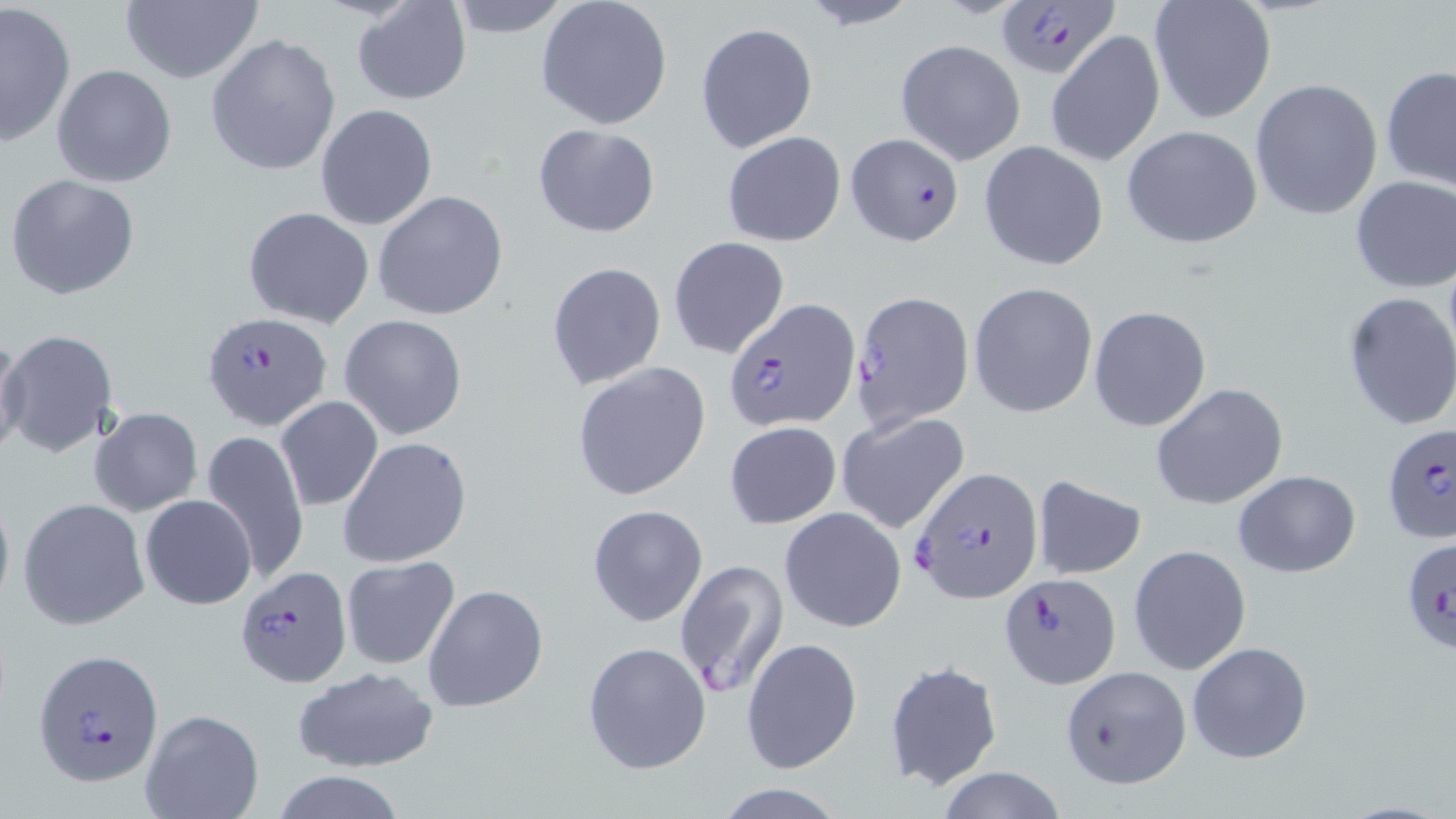 Approximate bounding boxes as named x1/y1/x2/y2 corners in pixels. Uninfected red blood cell locations: (x1=351, y1=0, x2=472, y2=105), (x1=444, y1=0, x2=574, y2=36), (x1=1149, y1=0, x2=1276, y2=123), (x1=0, y1=1, x2=76, y2=147), (x1=119, y1=1, x2=263, y2=85), (x1=536, y1=1, x2=672, y2=129), (x1=793, y1=2, x2=924, y2=30), (x1=695, y1=22, x2=818, y2=153), (x1=1046, y1=31, x2=1165, y2=167), (x1=205, y1=33, x2=342, y2=179), (x1=895, y1=39, x2=1025, y2=165), (x1=51, y1=64, x2=178, y2=187), (x1=1381, y1=64, x2=1456, y2=194), (x1=1250, y1=77, x2=1384, y2=221), (x1=314, y1=104, x2=438, y2=230), (x1=531, y1=123, x2=660, y2=238), (x1=1121, y1=125, x2=1264, y2=249), (x1=721, y1=131, x2=846, y2=246), (x1=979, y1=140, x2=1109, y2=271), (x1=6, y1=174, x2=140, y2=300), (x1=1350, y1=176, x2=1455, y2=292), (x1=372, y1=189, x2=510, y2=321), (x1=244, y1=206, x2=374, y2=327), (x1=666, y1=236, x2=790, y2=357), (x1=547, y1=261, x2=667, y2=392), (x1=968, y1=282, x2=1098, y2=417), (x1=1340, y1=291, x2=1456, y2=434), (x1=1088, y1=307, x2=1212, y2=431), (x1=340, y1=314, x2=467, y2=441), (x1=2, y1=329, x2=120, y2=458), (x1=0, y1=332, x2=28, y2=462), (x1=571, y1=362, x2=713, y2=500), (x1=1151, y1=382, x2=1288, y2=509), (x1=276, y1=396, x2=383, y2=511), (x1=88, y1=406, x2=203, y2=516), (x1=835, y1=412, x2=970, y2=534), (x1=724, y1=420, x2=842, y2=528), (x1=201, y1=430, x2=311, y2=582), (x1=338, y1=436, x2=472, y2=568), (x1=1233, y1=469, x2=1361, y2=578), (x1=1031, y1=476, x2=1146, y2=579), (x1=0, y1=482, x2=15, y2=619), (x1=140, y1=495, x2=257, y2=609), (x1=17, y1=497, x2=150, y2=631), (x1=587, y1=505, x2=708, y2=626), (x1=780, y1=507, x2=906, y2=633), (x1=1129, y1=545, x2=1252, y2=674), (x1=340, y1=556, x2=460, y2=671), (x1=673, y1=558, x2=788, y2=700), (x1=422, y1=584, x2=548, y2=712), (x1=741, y1=638, x2=862, y2=775), (x1=1186, y1=640, x2=1313, y2=764), (x1=582, y1=641, x2=711, y2=773), (x1=883, y1=660, x2=1004, y2=791), (x1=292, y1=666, x2=440, y2=773), (x1=140, y1=708, x2=263, y2=819), (x1=934, y1=765, x2=1070, y2=819), (x1=271, y1=771, x2=407, y2=819), (x1=710, y1=780, x2=853, y2=818). Plasmodium falciparum-infected red blood cell locations: (x1=994, y1=0, x2=1120, y2=82), (x1=845, y1=131, x2=963, y2=245), (x1=850, y1=288, x2=976, y2=433), (x1=729, y1=300, x2=860, y2=433), (x1=202, y1=312, x2=332, y2=431), (x1=1382, y1=422, x2=1456, y2=545), (x1=909, y1=466, x2=1044, y2=603), (x1=1401, y1=536, x2=1455, y2=659), (x1=235, y1=562, x2=352, y2=686), (x1=999, y1=571, x2=1120, y2=688), (x1=33, y1=647, x2=163, y2=787), (x1=1060, y1=665, x2=1191, y2=789). Slide-level diagnosis: Plasmodium falciparum. Light microscopy. May-Grünwald-Giemsa stain. 1000x magnification. Image is 1456×819 pixels. Thin blood film. Single field of view.